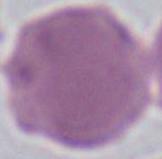 An erythrocyte is shown. Photomicrograph. 1000x magnification.